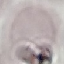
malaria status = uninfected
capture = smartphone camera at the microscope eyepiece
preparation = thin smear
stain = Giemsa
image type = cell patch, automatically extracted from a larger field of view and resized to 64 × 64 pixels